Name the parasite shown.
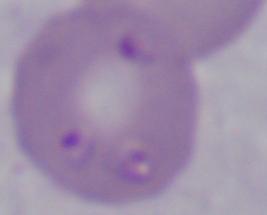
This is Babesia.

magnification = 1000x
modality = micrograph